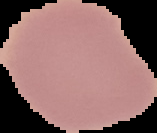
The area outside the segmented cell region is set to black. From a thin blood smear. Image is 157×133 pixels. Malaria status: uninfected.